Locate every uninfected red blood cell.
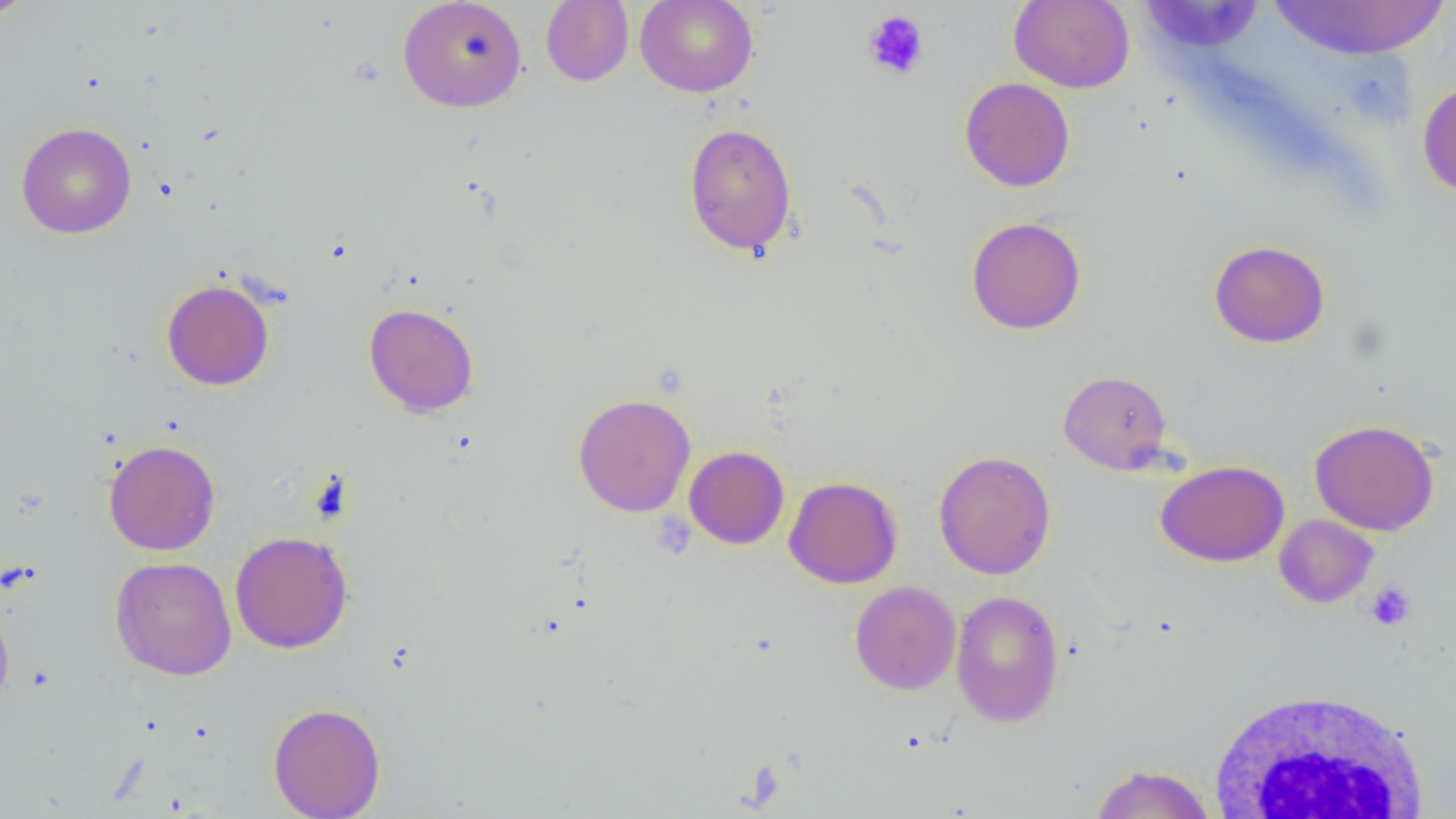

Approximate bounding boxes as (x1, y1, x2, y2) in pixels.
Uninfected red blood cells: (0, 0, 40, 22), (397, 0, 528, 113), (634, 0, 759, 98), (1268, 0, 1450, 60), (541, 1, 634, 86), (1009, 1, 1135, 93), (1140, 3, 1258, 56), (960, 77, 1075, 192), (1417, 80, 1456, 198), (683, 121, 797, 257), (15, 122, 136, 239), (966, 216, 1087, 334), (1208, 240, 1330, 348), (161, 279, 275, 390), (363, 302, 479, 417), (1059, 370, 1173, 474), (573, 393, 696, 517), (1310, 419, 1439, 536), (103, 439, 220, 555), (684, 445, 790, 549), (933, 450, 1056, 580), (1155, 460, 1289, 567), (784, 476, 902, 589), (1275, 515, 1378, 607), (230, 531, 353, 653), (110, 556, 237, 680), (850, 581, 961, 695), (950, 590, 1065, 727), (0, 599, 15, 714), (268, 702, 385, 819), (1088, 763, 1216, 818).

Platelet locations: (862, 10, 929, 81), (652, 512, 696, 559), (1365, 582, 1416, 631). White blood cell locations: (1206, 687, 1434, 819). Slide-level diagnosis: no evidence of blood parasites. Captured at 1000x magnification. Image is 1456×819 pixels. Thin blood smear. One field of a larger specimen. Optical microscopy.